Assess this cell for malaria.
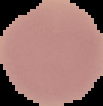

It is uninfected.

Summary:
  - Image size: 103×106 pixels
  - Image type: segmented cell region with the area outside set to black
  - Preparation: thin blood film